Name the blood parasite species.
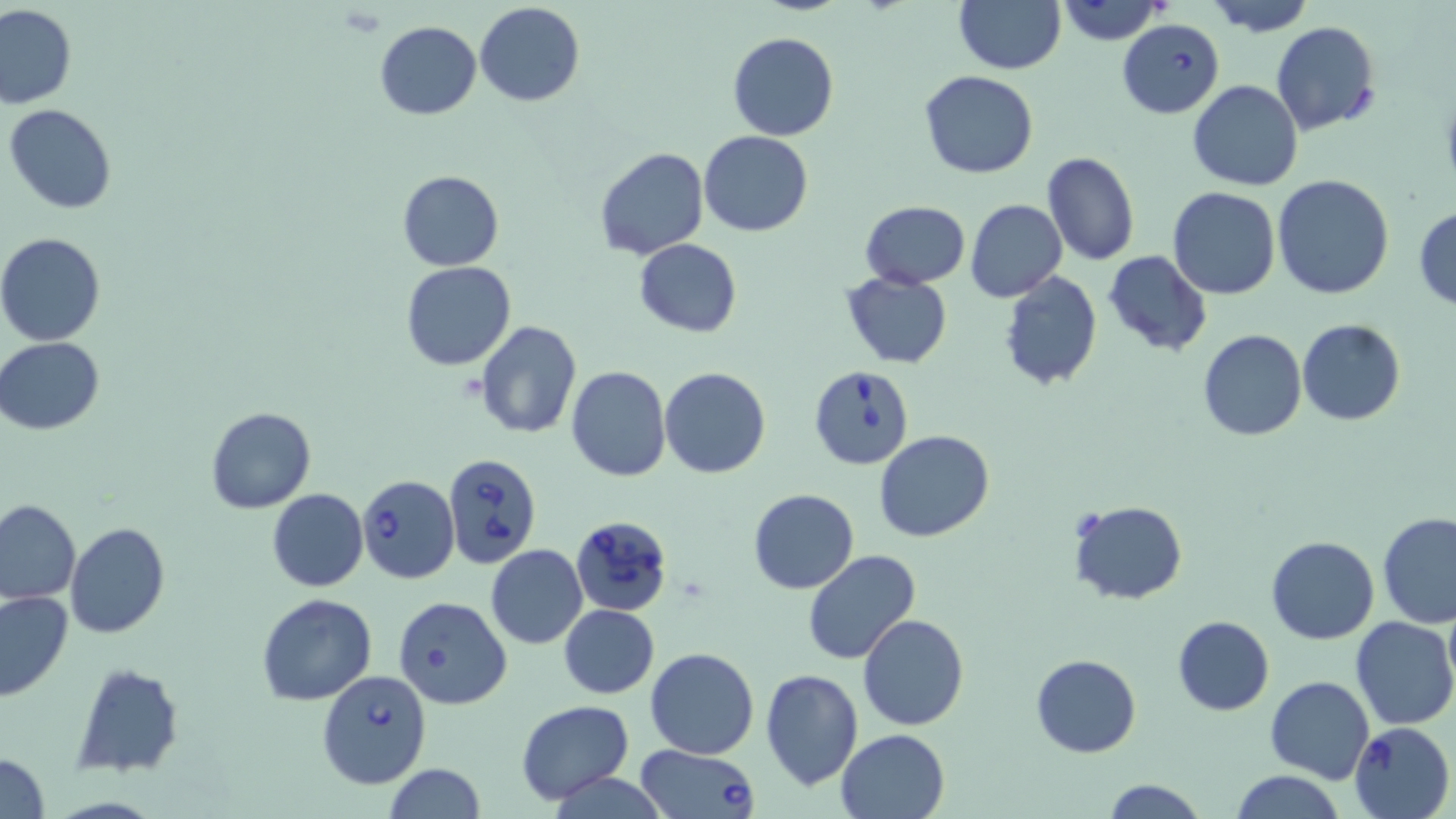

Babesia divergens.

Summary:
  - Coordinate format: approximate bounding boxes as (x1,y1)-(x2,y2) corner pairs in pixels
  - Uninfected red blood cell locations: (1052,0)-(1168,46), (1201,0)-(1317,35), (954,1)-(1065,74), (474,2)-(586,106), (0,3)-(77,109), (374,19)-(482,119), (1270,22)-(1381,135), (728,31)-(839,141), (919,70)-(1038,179), (1188,80)-(1303,191), (5,104)-(117,215), (700,130)-(813,237), (593,147)-(708,261), (1041,151)-(1141,266), (397,170)-(504,271), (1272,174)-(1396,300), (1168,187)-(1281,299), (862,199)-(969,288), (966,199)-(1068,303), (1413,204)-(1456,308), (0,233)-(106,346), (634,238)-(741,338), (1103,250)-(1212,358), (401,261)-(516,370), (998,269)-(1102,392), (841,270)-(953,370), (1297,319)-(1406,426), (475,320)-(582,438), (1197,329)-(1307,442), (0,337)-(106,435), (566,365)-(672,482), (660,367)-(771,479), (206,406)-(315,513), (876,431)-(994,543), (266,488)-(368,592), (748,489)-(858,593), (0,499)-(80,603), (1067,500)-(1187,604), (1377,511)-(1456,628), (65,522)-(170,639), (1266,535)-(1379,643), (486,544)-(588,650), (802,549)-(920,665), (0,590)-(73,703), (257,594)-(378,706), (393,596)-(511,709), (1442,596)-(1456,708), (559,604)-(659,698), (859,612)-(969,730), (1172,616)-(1275,715), (1350,617)-(1456,730), (646,647)-(759,760), (1030,653)-(1141,757), (71,661)-(182,773), (761,668)-(862,791), (1265,676)-(1374,781), (516,699)-(634,803), (1349,721)-(1454,819), (835,728)-(949,818), (0,752)-(50,819), (384,764)-(487,819), (1228,770)-(1347,819), (549,772)-(667,819), (1099,777)-(1207,819)
  - Babesia divergens-infected red blood cell locations: (1117,19)-(1224,118), (808,364)-(913,471), (443,453)-(543,570), (356,473)-(460,584), (570,514)-(674,619), (317,670)-(430,788), (632,743)-(762,819)
  - Magnification: 1000x
  - Modality: light microscopy
  - Field of view: single
  - Preparation: thin blood film
  - Stain: May-Grünwald-Giemsa
  - Image size: 1456×819 pixels